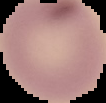
Malaria status: uninfected. From a thin blood smear. Image is 106×103 pixels. Cell region segmented out of the field of view; the surrounding area is masked to black.